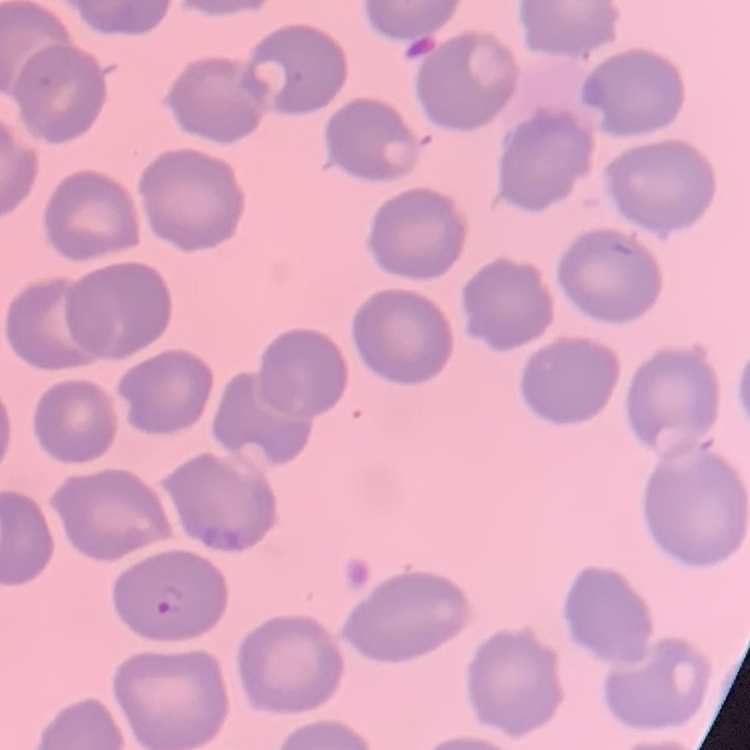

Summary:
  - Erythrocyte morphology: no rouleaux formation
  - Stain: Field's or Giemsa
  - Image type: square crop of a larger photomicrograph
  - Preparation: thin peripheral smear